Outline each blood parasite and name the species.
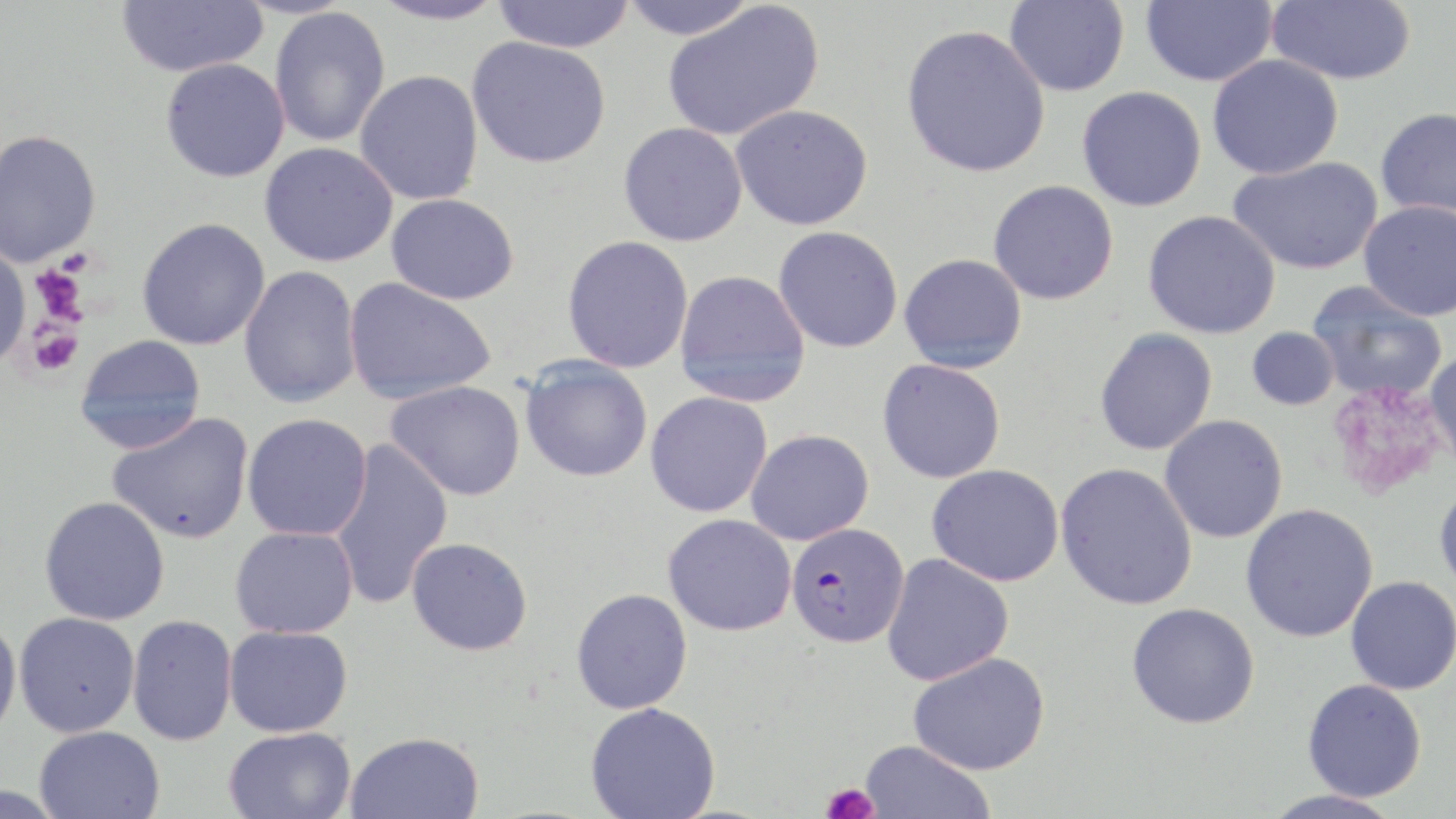

Approximate bounding boxes as named x1/y1/x2/y2 corners in pixels.
Plasmodium falciparum-infected red blood cells: (x1=786, y1=522, x2=909, y2=647).
No Plasmodium ovale, Plasmodium malariae, Plasmodium vivax, Babesia divergens, or Trypanosoma brucei observed.

Uninfected red blood cell locations: (x1=116, y1=0, x2=268, y2=77), (x1=367, y1=0, x2=508, y2=26), (x1=491, y1=0, x2=637, y2=53), (x1=618, y1=0, x2=760, y2=40), (x1=1140, y1=0, x2=1277, y2=87), (x1=1266, y1=0, x2=1416, y2=86), (x1=1004, y1=1, x2=1130, y2=97), (x1=662, y1=2, x2=825, y2=142), (x1=269, y1=6, x2=390, y2=147), (x1=901, y1=24, x2=1051, y2=178), (x1=467, y1=36, x2=612, y2=169), (x1=1207, y1=55, x2=1344, y2=179), (x1=160, y1=59, x2=290, y2=183), (x1=354, y1=70, x2=484, y2=205), (x1=1077, y1=86, x2=1207, y2=211), (x1=731, y1=104, x2=873, y2=231), (x1=1375, y1=107, x2=1456, y2=221), (x1=618, y1=122, x2=748, y2=246), (x1=0, y1=129, x2=102, y2=268), (x1=259, y1=142, x2=398, y2=267), (x1=1228, y1=156, x2=1383, y2=275), (x1=988, y1=180, x2=1119, y2=305), (x1=386, y1=193, x2=520, y2=305), (x1=1359, y1=200, x2=1456, y2=321), (x1=1143, y1=210, x2=1281, y2=339), (x1=137, y1=217, x2=271, y2=351), (x1=773, y1=226, x2=903, y2=353), (x1=561, y1=235, x2=694, y2=374), (x1=0, y1=244, x2=30, y2=368), (x1=899, y1=253, x2=1027, y2=373), (x1=239, y1=265, x2=362, y2=408), (x1=674, y1=269, x2=811, y2=407), (x1=343, y1=278, x2=497, y2=405), (x1=1307, y1=281, x2=1448, y2=402), (x1=1246, y1=327, x2=1340, y2=411), (x1=1094, y1=328, x2=1217, y2=455), (x1=75, y1=335, x2=206, y2=454), (x1=1425, y1=348, x2=1456, y2=473), (x1=520, y1=357, x2=653, y2=482), (x1=877, y1=359, x2=1006, y2=483), (x1=385, y1=380, x2=526, y2=501), (x1=645, y1=391, x2=773, y2=518), (x1=106, y1=412, x2=255, y2=543), (x1=242, y1=413, x2=372, y2=541), (x1=1159, y1=415, x2=1288, y2=543), (x1=745, y1=429, x2=874, y2=545), (x1=329, y1=439, x2=453, y2=609), (x1=1055, y1=462, x2=1198, y2=611), (x1=927, y1=464, x2=1064, y2=586), (x1=1434, y1=479, x2=1456, y2=598), (x1=39, y1=496, x2=170, y2=626), (x1=1240, y1=503, x2=1378, y2=643), (x1=663, y1=514, x2=796, y2=636), (x1=230, y1=526, x2=358, y2=639), (x1=406, y1=536, x2=533, y2=655), (x1=882, y1=553, x2=1014, y2=686), (x1=1345, y1=576, x2=1456, y2=695), (x1=571, y1=588, x2=693, y2=714), (x1=1127, y1=602, x2=1260, y2=729), (x1=14, y1=612, x2=140, y2=737), (x1=0, y1=613, x2=22, y2=744), (x1=127, y1=615, x2=238, y2=746), (x1=224, y1=625, x2=353, y2=737), (x1=909, y1=652, x2=1050, y2=775), (x1=1301, y1=679, x2=1427, y2=802), (x1=585, y1=702, x2=721, y2=819), (x1=35, y1=725, x2=164, y2=818), (x1=223, y1=727, x2=356, y2=819), (x1=345, y1=731, x2=484, y2=819), (x1=859, y1=740, x2=995, y2=819), (x1=1260, y1=788, x2=1404, y2=819). Platelet locations: (x1=30, y1=264, x2=89, y2=325), (x1=26, y1=320, x2=83, y2=375), (x1=1326, y1=382, x2=1447, y2=501), (x1=821, y1=782, x2=879, y2=819). Slide-level diagnosis: Plasmodium falciparum. May-Grünwald-Giemsa-stained preparation. Single field of view. Light microscopy. Thin blood film. Image is 1456×819 pixels. Captured at 1000x magnification.